Describe the morphology of the erythrocytes.
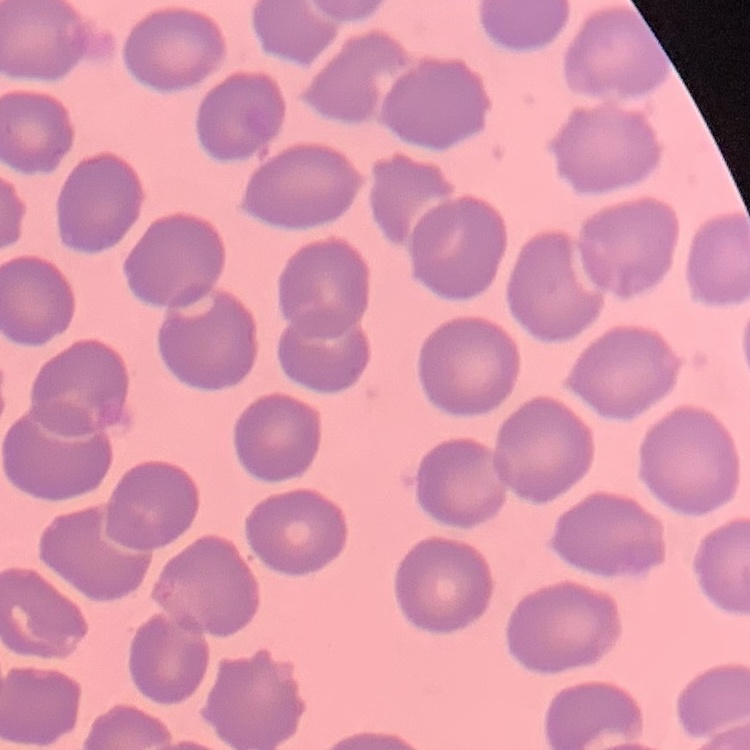
They show no rouleaux formation.

Stained with either Field's or Giemsa. Thin peripheral smear. Square crop of a larger photomicrograph.